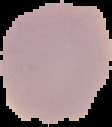

Malaria status: uninfected. From a thin blood smear. The area outside the segmented cell region is set to black. Image is 112×127 pixels.